Give the extent of all Plasmodium vivax-infected red blood cells.
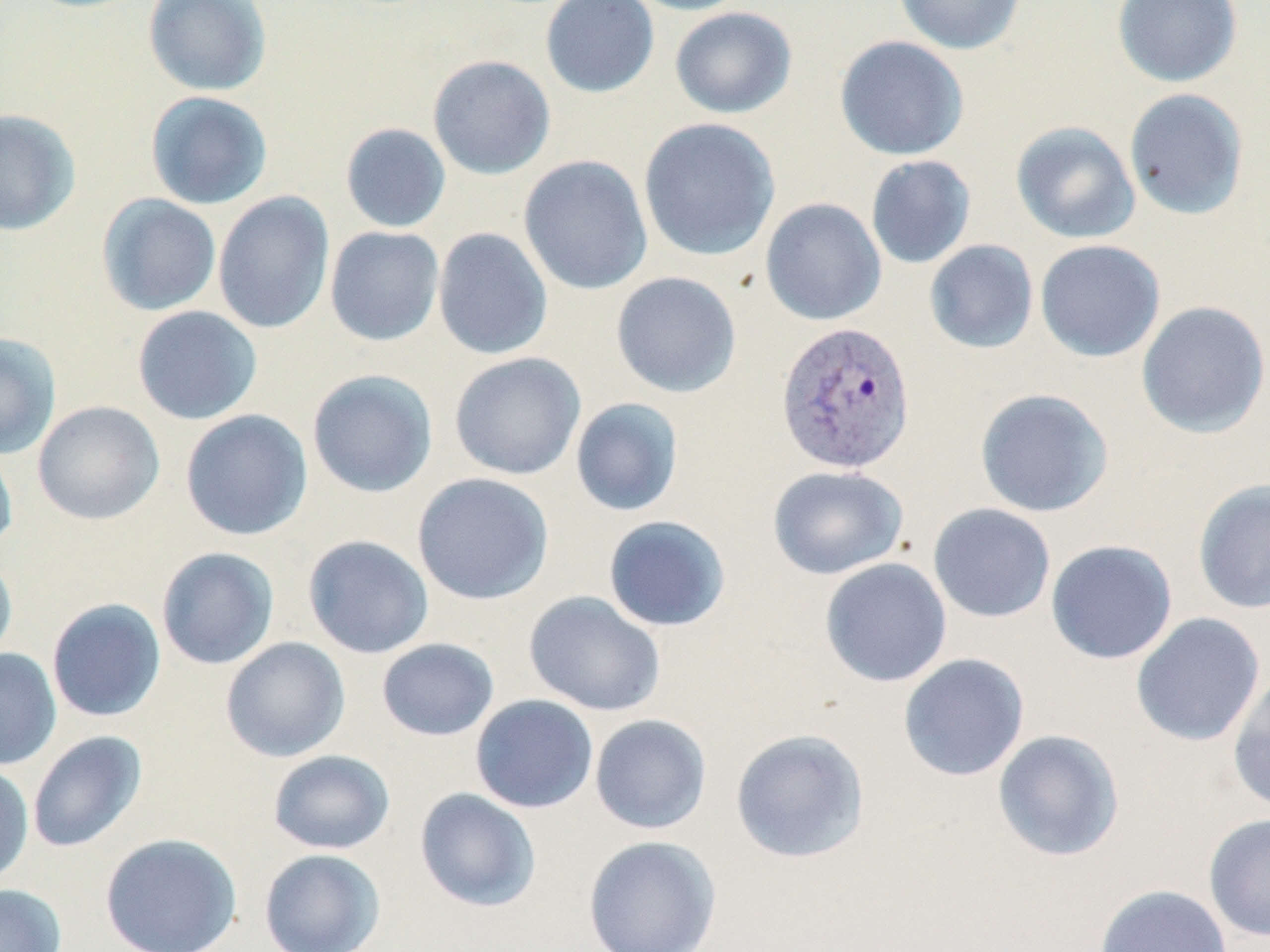

Approximate bounding boxes as (x1, y1, x2, y2) in pixels.
Plasmodium vivax-infected red blood cells: (776, 320, 917, 475).

Uninfected red blood cell locations: (142, 0, 272, 97), (540, 0, 660, 98), (625, 0, 754, 16), (894, 0, 1026, 55), (1112, 0, 1243, 87), (670, 6, 797, 119), (834, 36, 969, 161), (427, 54, 556, 180), (1124, 88, 1249, 221), (145, 91, 274, 210), (0, 108, 81, 236), (638, 117, 780, 262), (1011, 121, 1140, 243), (340, 123, 451, 233), (518, 155, 653, 296), (865, 155, 976, 269), (212, 191, 335, 335), (97, 194, 222, 316), (760, 198, 886, 326), (325, 226, 444, 346), (433, 228, 553, 360), (1035, 239, 1166, 362), (924, 240, 1039, 354), (610, 271, 742, 398), (1136, 300, 1270, 438), (132, 305, 263, 425), (0, 332, 62, 459), (449, 352, 585, 480), (307, 369, 438, 498), (975, 388, 1114, 518), (570, 398, 684, 517), (32, 400, 165, 525), (180, 409, 313, 541), (0, 438, 18, 554), (767, 465, 908, 580), (412, 473, 554, 605), (1192, 479, 1270, 614), (927, 503, 1056, 624), (603, 515, 731, 632), (302, 535, 434, 659), (1045, 539, 1178, 665), (156, 546, 279, 670), (0, 553, 18, 666), (819, 557, 952, 687), (524, 590, 666, 716), (46, 598, 166, 722), (1130, 612, 1266, 747), (220, 637, 350, 762), (376, 638, 499, 741), (0, 648, 61, 771), (897, 653, 1030, 781), (1227, 672, 1270, 816), (470, 694, 598, 813), (589, 714, 712, 835), (730, 727, 870, 864), (992, 729, 1125, 862), (27, 731, 147, 853), (268, 749, 395, 855), (0, 763, 34, 885), (414, 788, 541, 912), (1203, 812, 1270, 942), (99, 832, 242, 952), (583, 835, 722, 952), (258, 848, 386, 952), (0, 884, 66, 951), (1094, 884, 1232, 952). Slide-level diagnosis: Plasmodium vivax. May-Grünwald-Giemsa-stained preparation. Thin blood smear. Image is 1270×952 pixels. Light microscopy. Single field of view. 1000x magnification.